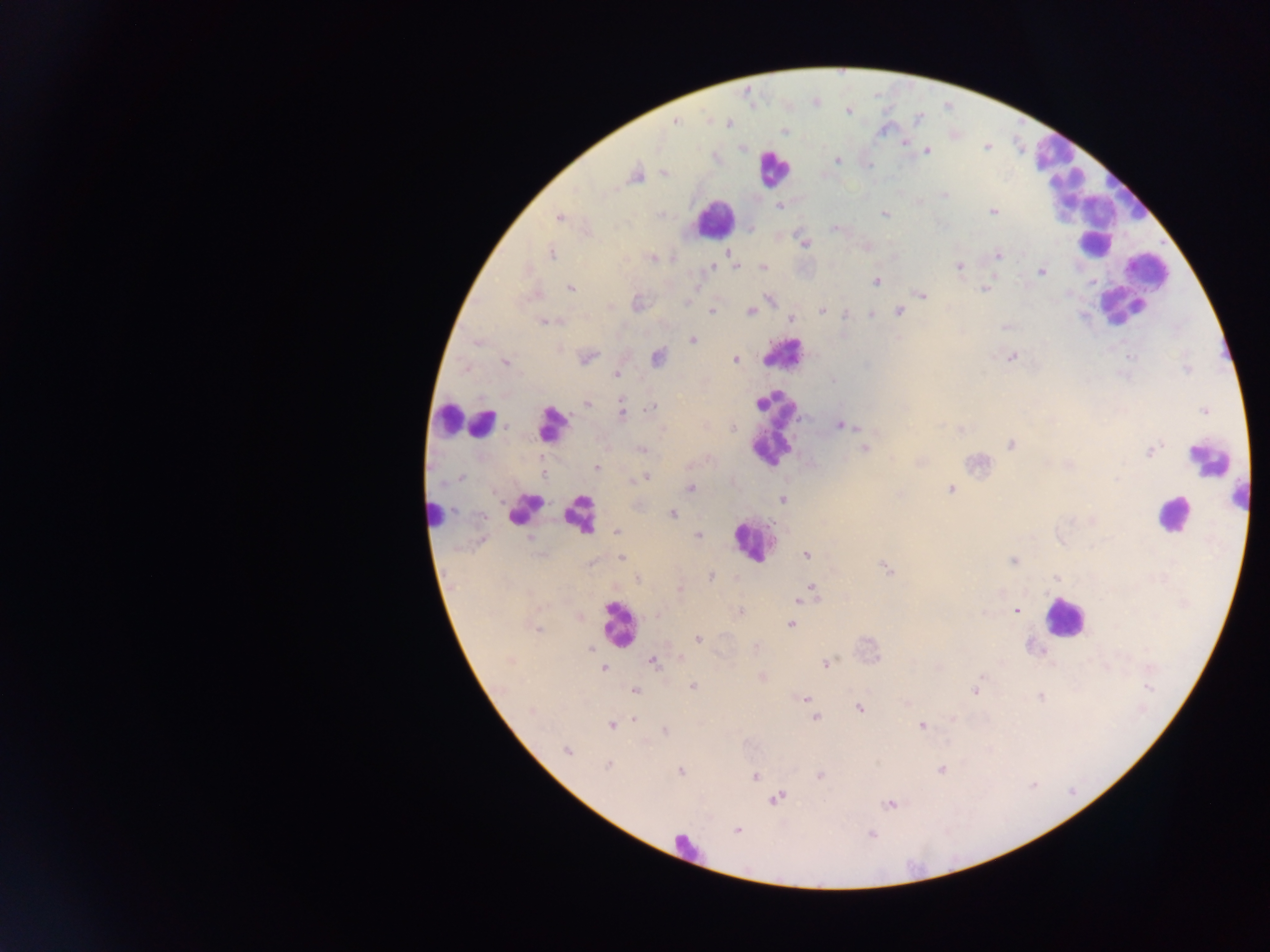

Approximate centers as (x, y) in pixels.
Summary:
  - Malaria parasite locations: (813, 101), (848, 110), (674, 121), (728, 122), (783, 130), (903, 142), (742, 147), (927, 150), (837, 161), (664, 172), (636, 176), (944, 194), (779, 205), (994, 211), (884, 214), (559, 217), (835, 227), (751, 228), (805, 243), (866, 246), (726, 251), (550, 252), (997, 254), (652, 258), (958, 265), (735, 266), (711, 267), (762, 267), (1041, 271), (994, 274), (875, 281), (570, 288), (985, 290), (534, 295), (922, 295), (769, 299), (686, 301), (637, 303), (821, 311), (899, 311), (711, 312), (749, 312), (870, 314), (845, 315), (791, 319), (548, 322), (1005, 327), (693, 339), (477, 342), (586, 357), (1011, 357), (657, 358), (734, 359), (505, 361), (615, 374), (587, 403), (651, 408), (1204, 410), (622, 412), (839, 424), (960, 429), (1012, 445), (864, 447), (640, 449), (1150, 450), (920, 462), (597, 467), (542, 473), (647, 476), (461, 477), (631, 480), (690, 488), (950, 489), (782, 498), (670, 513), (617, 532), (698, 535), (806, 555), (621, 557), (1013, 560), (885, 567), (710, 576), (638, 578), (1056, 578), (679, 588), (811, 593), (801, 598), (1016, 611), (739, 612), (578, 615), (790, 624), (537, 628), (698, 638), (591, 647), (757, 647), (679, 659), (511, 661), (652, 661), (825, 664), (603, 668), (761, 677), (694, 686), (975, 690), (635, 691), (1041, 696), (806, 699), (909, 702), (858, 708), (632, 718), (815, 718), (952, 719), (611, 725), (921, 725), (665, 730), (566, 750), (608, 766), (941, 769), (680, 771), (820, 775), (755, 776), (776, 798), (889, 803), (737, 830), (871, 834)
  - Leukocyte locations: (1051, 152), (772, 167), (1096, 206), (714, 220), (1094, 243), (1148, 272), (1124, 307), (782, 353), (447, 418), (482, 423), (551, 423), (771, 430), (1210, 459), (1243, 493), (525, 509), (1173, 513), (434, 514), (580, 514), (753, 541), (1064, 618), (617, 624), (687, 848)
  - Preparation: thick blood smear
  - Capture: mobile-phone photograph through a microscope
  - Image size: 1270×952 pixels
  - Country: Ghana
  - Field of view: single